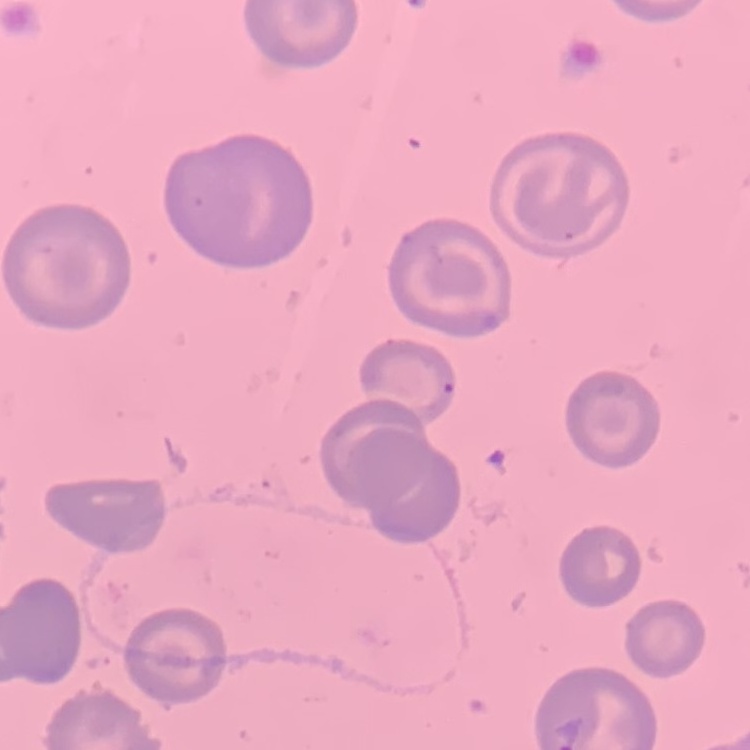
Summary:
  - Erythrocyte morphology: no rouleaux formation
  - Image type: square crop of a larger photomicrograph
  - Preparation: thin peripheral smear
  - Stain: Field's or Giemsa